Locate and identify every blood parasite.
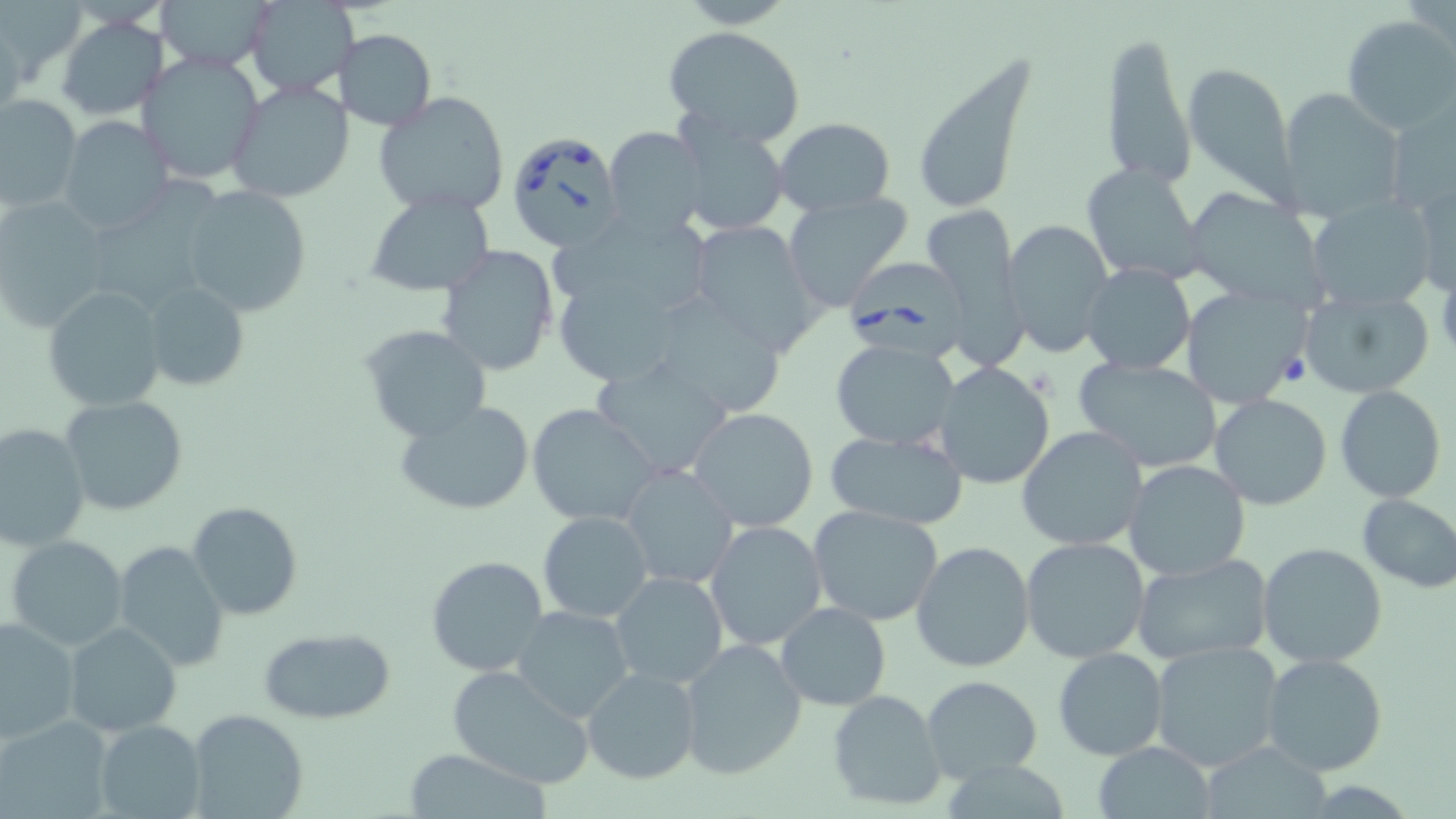
Approximate bounding boxes as (x1,y1)-(x2,y2) corner pairs in pixels.
Babesia divergens-infected red blood cells: (506,129)-(624,250), (845,256)-(975,363).
No Plasmodium falciparum, Plasmodium ovale, Plasmodium malariae, Plasmodium vivax, or Trypanosoma brucei observed.

{
  "slide_level_diagnosis": "Babesia divergens",
  "magnification": "1000x",
  "preparation": "thin blood film",
  "field_of_view": "one of a larger specimen",
  "modality": "light microscopy",
  "image_size": "1456×819 pixels",
  "stain": "May-Grünwald-Giemsa",
  "uninfected_red_blood_cell_locations": "approximate bounding boxes as (x1,y1)-(x2,y2) corner pairs in pixels: (158,0)-(271,70), (244,1)-(356,97), (1342,14)-(1456,134), (57,16)-(168,120), (664,25)-(805,146), (336,30)-(436,130), (1099,31)-(1195,191), (911,50)-(1036,218), (138,51)-(266,185), (1183,60)-(1300,205), (227,80)-(352,204), (1278,88)-(1407,223), (373,91)-(511,217), (0,93)-(83,215), (59,116)-(175,237), (677,118)-(790,235), (774,118)-(894,215), (603,126)-(710,237), (1080,163)-(1205,283), (95,173)-(238,310), (1414,174)-(1455,303), (1186,185)-(1327,310), (181,187)-(311,316), (365,191)-(494,295), (783,193)-(914,310), (1307,196)-(1437,311), (0,197)-(111,331), (921,203)-(1022,358), (546,213)-(713,314), (1003,217)-(1115,358), (687,221)-(824,355), (437,243)-(559,377), (1081,263)-(1195,373), (559,277)-(683,391), (141,282)-(251,391), (1178,283)-(1307,407), (43,286)-(165,411), (1295,289)-(1433,401), (647,294)-(788,419), (360,324)-(491,442), (831,339)-(960,450), (1074,356)-(1222,472), (590,357)-(736,480), (931,362)-(1056,488), (1335,384)-(1446,502), (1208,393)-(1332,511), (61,394)-(187,516), (395,399)-(535,517), (527,404)-(660,528), (688,407)-(820,531), (0,421)-(90,551), (1017,425)-(1147,553), (823,428)-(967,530), (1123,459)-(1251,580), (621,464)-(738,589), (1356,491)-(1456,593), (188,501)-(303,620), (809,506)-(945,626), (537,510)-(652,623), (705,520)-(828,652), (7,535)-(128,650), (1019,537)-(1150,663), (912,540)-(1036,671), (112,541)-(229,670), (1258,542)-(1388,667), (426,555)-(548,678), (1130,555)-(1273,666), (610,572)-(728,690), (774,602)-(890,711), (510,605)-(636,722), (1,617)-(79,743), (64,620)-(182,738), (258,629)-(397,725), (678,639)-(807,779), (1148,640)-(1285,772), (1052,647)-(1168,760), (1261,653)-(1389,776), (445,665)-(597,789), (582,667)-(701,784), (920,675)-(1042,784), (826,688)-(949,812), (185,708)-(308,819), (0,714)-(112,819), (94,719)-(206,819), (1197,741)-(1331,817), (1093,742)-(1215,818), (402,747)-(551,819), (936,760)-(1077,817)"
}